Locate every Plasmodium parasite.
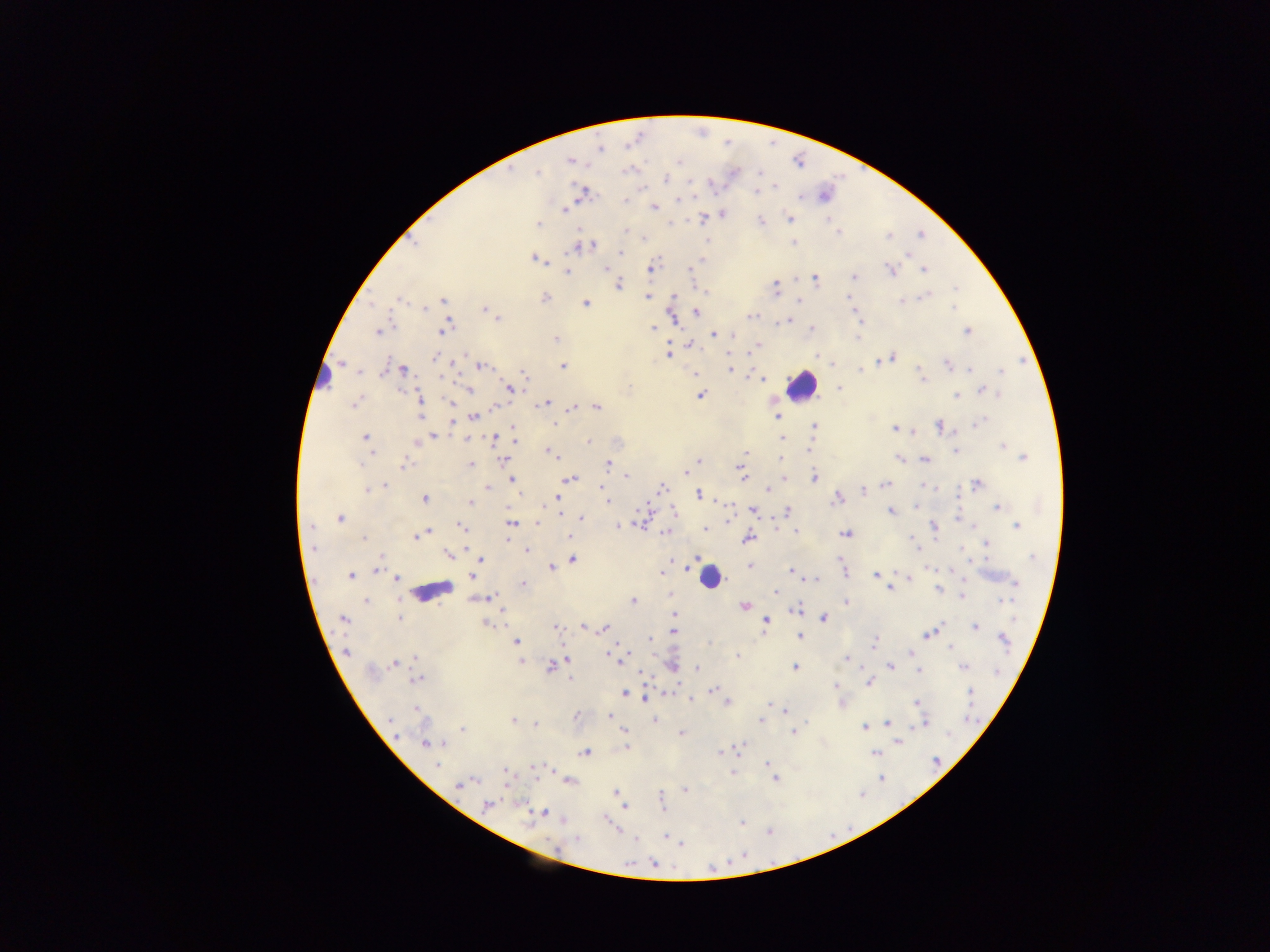
Approximate centers as {x, y} in pixels.
Plasmodium parasites: {600, 149}, {570, 161}, {759, 172}, {537, 173}, {664, 179}, {711, 184}, {774, 187}, {757, 191}, {583, 193}, {799, 196}, {678, 199}, {626, 201}, {655, 207}, {565, 209}, {723, 213}, {703, 218}, {789, 218}, {761, 222}, {538, 223}, {626, 230}, {838, 232}, {888, 236}, {794, 243}, {590, 246}, {582, 247}, {574, 248}, {621, 252}, {535, 259}, {701, 262}, {605, 267}, {650, 268}, {924, 269}, {691, 270}, {891, 270}, {567, 271}, {854, 276}, {815, 278}, {619, 284}, {775, 287}, {956, 287}, {926, 296}, {647, 297}, {544, 298}, {400, 301}, {442, 301}, {799, 301}, {901, 301}, {585, 304}, {424, 308}, {953, 308}, {487, 310}, {696, 312}, {493, 314}, {856, 314}, {751, 316}, {671, 317}, {496, 318}, {787, 321}, {445, 328}, {653, 328}, {812, 328}, {967, 331}, {377, 332}, {712, 335}, {733, 335}, {556, 338}, {690, 345}, {758, 345}, {669, 354}, {816, 357}, {892, 357}, {436, 358}, {880, 359}, {481, 365}, {947, 365}, {563, 367}, {731, 369}, {861, 369}, {971, 369}, {402, 370}, {1001, 372}, {523, 374}, {696, 374}, {762, 379}, {922, 379}, {839, 387}, {510, 389}, {469, 391}, {984, 391}, {993, 393}, {701, 395}, {956, 395}, {999, 395}, {420, 399}, {450, 402}, {544, 403}, {353, 404}, {494, 406}, {597, 407}, {572, 408}, {420, 416}, {474, 416}, {777, 416}, {980, 421}, {452, 422}, {556, 425}, {939, 425}, {814, 426}, {895, 428}, {512, 430}, {433, 435}, {514, 435}, {366, 437}, {468, 438}, {781, 438}, {494, 440}, {589, 442}, {417, 443}, {1003, 446}, {548, 450}, {807, 450}, {955, 451}, {745, 453}, {553, 455}, {1022, 457}, {780, 459}, {899, 459}, {925, 459}, {504, 460}, {699, 461}, {608, 463}, {360, 464}, {404, 464}, {470, 465}, {686, 472}, {742, 474}, {626, 476}, {783, 477}, {814, 477}, {571, 479}, {511, 480}, {886, 484}, {977, 484}, {384, 485}, {924, 486}, {487, 488}, {601, 488}, {661, 489}, {368, 490}, {769, 490}, {864, 491}, {699, 494}, {557, 497}, {838, 498}, {424, 499}, {607, 500}, {469, 502}, {996, 507}, {753, 510}, {675, 511}, {788, 511}, {559, 512}, {891, 512}, {582, 518}, {340, 519}, {464, 519}, {640, 522}, {511, 523}, {538, 523}, {776, 524}, {310, 526}, {618, 526}, {933, 526}, {971, 526}, {1017, 526}, {461, 527}, {706, 529}, {797, 531}, {427, 532}, {666, 532}, {845, 533}, {418, 536}, {569, 537}, {363, 538}, {748, 538}, {913, 540}, {987, 544}, {313, 547}, {916, 547}, {962, 550}, {526, 551}, {448, 555}, {1033, 557}, {480, 560}, {572, 560}, {749, 565}, {551, 567}, {377, 571}, {476, 571}, {791, 571}, {662, 572}, {844, 572}, {877, 574}, {351, 576}, {472, 576}, {908, 578}, {396, 579}, {812, 579}, {1015, 583}, {523, 585}, {890, 589}, {938, 590}, {776, 592}, {962, 596}, {489, 597}, {1005, 599}, {365, 602}, {633, 602}, {846, 602}, {744, 606}, {796, 609}, {674, 614}, {823, 617}, {399, 618}, {343, 619}, {766, 621}, {486, 623}, {975, 626}, {583, 627}, {588, 627}, {556, 628}, {604, 628}, {673, 631}, {928, 634}, {800, 637}, {650, 639}, {1004, 640}, {515, 642}, {874, 643}, {951, 646}, {347, 651}, {910, 653}, {612, 655}, {737, 656}, {415, 658}, {617, 658}, {567, 659}, {846, 659}, {521, 662}, {394, 663}, {550, 666}, {672, 666}, {891, 666}, {794, 667}, {963, 667}, {698, 668}, {919, 670}, {997, 671}, {570, 679}, {416, 680}, {869, 683}, {836, 685}, {713, 690}, {971, 692}, {624, 693}, {647, 699}, {690, 699}, {729, 702}, {917, 702}, {416, 708}, {785, 712}, {577, 714}, {609, 716}, {654, 720}, {761, 720}, {513, 721}, {923, 722}, {535, 724}, {888, 724}, {863, 728}, {462, 729}, {624, 732}, {794, 732}, {682, 733}, {899, 742}, {425, 744}, {626, 747}, {739, 747}, {726, 751}, {720, 752}, {585, 753}, {874, 753}, {767, 764}, {437, 765}, {535, 767}, {505, 772}, {732, 772}, {775, 779}, {881, 779}, {571, 781}, {468, 783}, {460, 785}, {686, 790}, {615, 793}, {661, 797}, {660, 803}, {488, 805}, {624, 807}, {543, 813}, {741, 823}, {768, 832}, {665, 836}, {635, 839}, {578, 840}, {681, 844}, {653, 863}.

Leukocyte locations: {324, 378}, {802, 385}, {710, 579}, {432, 590}. Thick blood smear. Single field of view. Collected in Ghana. Mobile-phone photograph taken through the microscope. Image is 1270×952 pixels.